Give the extent of all uninfected red blood cells.
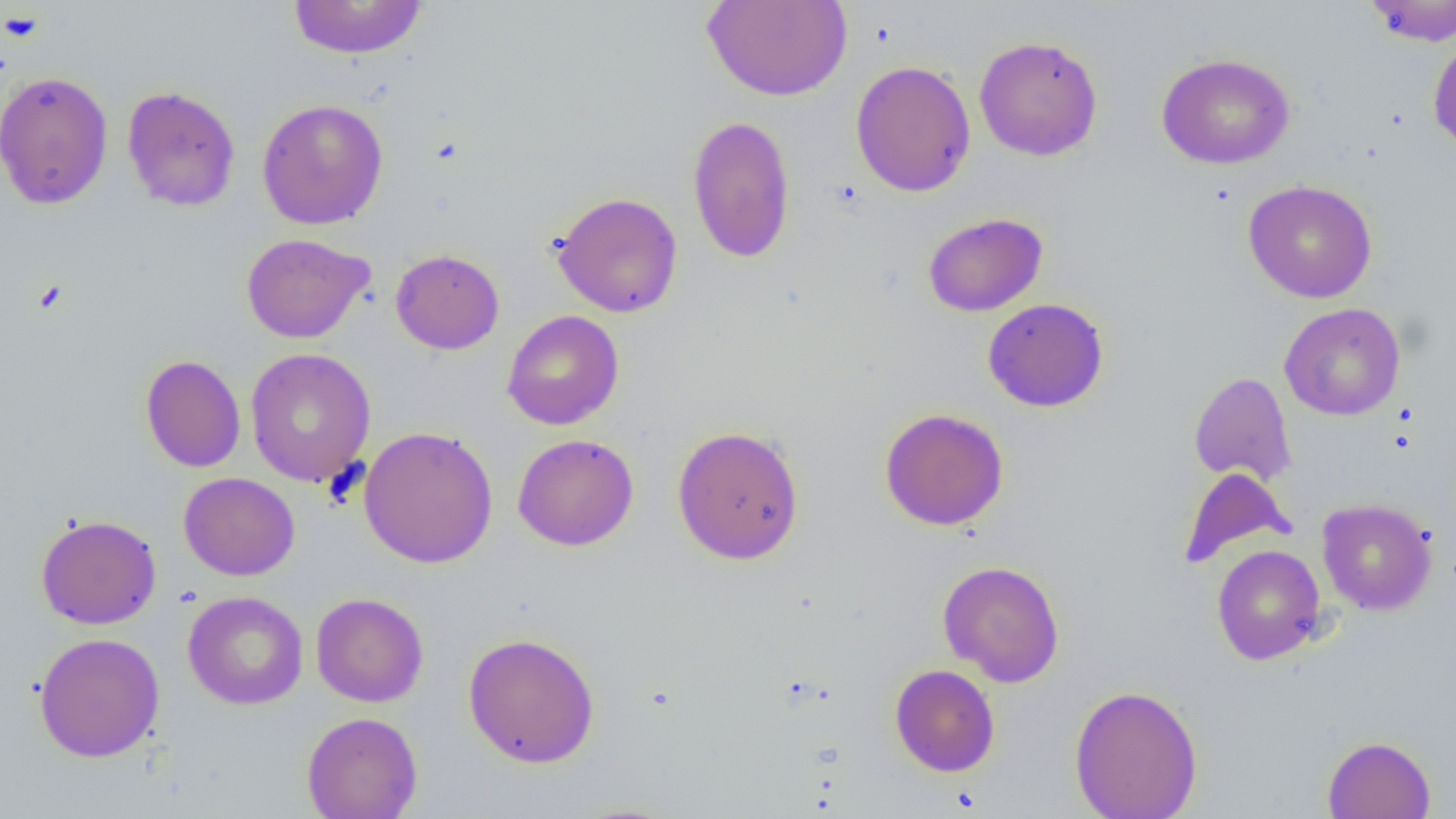

Approximate bounding boxes as (x1, y1, x2, y2) in pixels.
Uninfected red blood cells: (288, 0, 429, 59), (702, 0, 852, 102), (1364, 0, 1456, 46), (974, 35, 1103, 161), (1427, 35, 1456, 153), (1156, 52, 1295, 169), (850, 60, 976, 197), (0, 69, 114, 210), (122, 85, 241, 212), (257, 98, 389, 230), (687, 114, 796, 264), (1243, 180, 1377, 303), (551, 191, 684, 318), (922, 212, 1048, 317), (241, 233, 374, 343), (390, 249, 504, 355), (982, 298, 1109, 412), (1279, 302, 1406, 421), (502, 310, 624, 430), (245, 347, 376, 487), (140, 355, 246, 473), (1188, 371, 1297, 487), (879, 407, 1009, 531), (672, 424, 805, 565), (359, 425, 498, 569), (512, 433, 639, 551), (1177, 467, 1294, 568), (178, 472, 300, 581), (1317, 498, 1437, 615), (35, 515, 162, 630), (1212, 544, 1326, 665), (937, 559, 1065, 687), (182, 591, 308, 709), (311, 592, 428, 707), (463, 631, 600, 768), (34, 632, 165, 762), (889, 663, 1000, 776), (1069, 684, 1203, 819), (302, 711, 422, 819), (1322, 735, 1436, 819).

Platelet locations: (1, 10, 44, 44). Slide-level diagnosis: no evidence of blood parasites. Single field of view. Image is 1456×819 pixels. Thin blood film. Captured at 1000x magnification. Light microscopy.